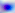
400x magnification. Micrograph. Toxoplasma gondii is shown.